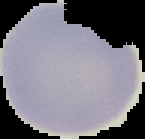

{
  "image_size": "145×139 pixels",
  "image_type": "segmented cell region on a black background",
  "preparation": "thin blood smear",
  "result": "no Plasmodium parasites detected"
}